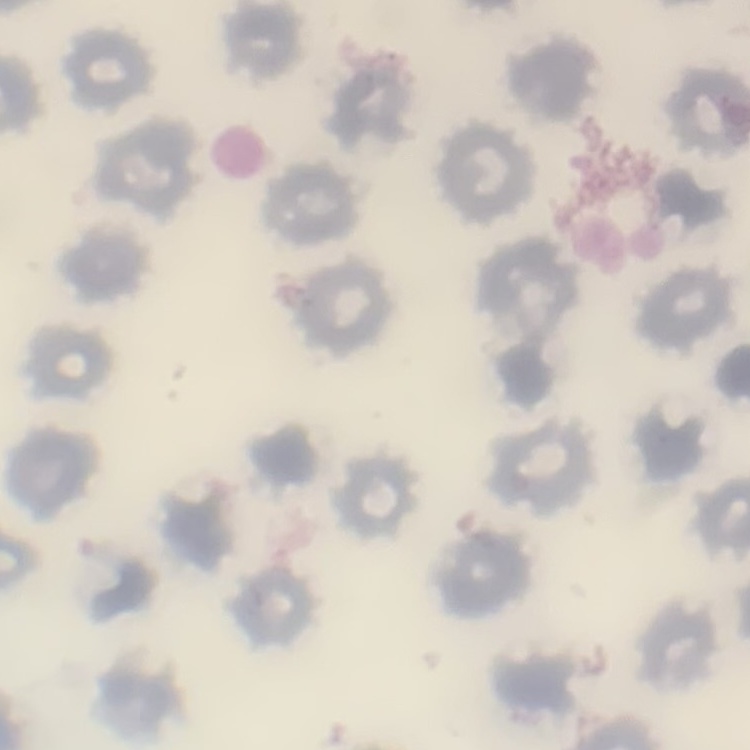
Summary:
  - Erythrocyte morphology: no rouleaux formation
  - Preparation: thin blood smear
  - Image type: square crop of a larger photomicrograph
  - Stain: Field's or Giemsa